Assess this cell for malaria.
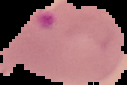

It is parasitized.

image type = cell region segmented out of the field of view; surrounding area masked to black
image size = 127×85 pixels
preparation = thin blood film